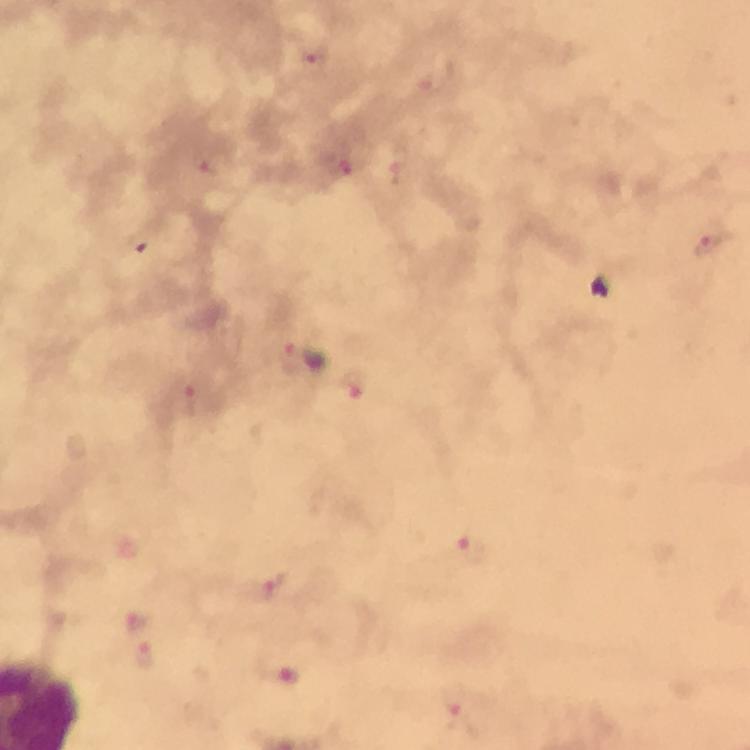

cropped_from: a single field of view
stain: Giemsa
preparation: thick smear
immersion_oil: used
malaria_parasite_locations: 'approximate centers as (x, y) in pixels: (314, 58), (207, 161), (338, 165), (711, 243), (295, 358), (352, 385), (188, 400), (470, 551), (271, 588), (141, 622), (146, 654), (456, 707)'
image_size: 750×750 pixels
capture: smartphone camera through the microscope
magnification: 100x
context: from a diagnostic examination for malaria